Classify this cell by malaria status.
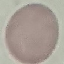

It is uninfected.

Summary:
  - Stain: Giemsa
  - Image type: cell patch, automatically extracted from a larger field of view and resized to 64 × 64 pixels
  - Capture: smartphone camera at the microscope eyepiece
  - Preparation: thin blood film